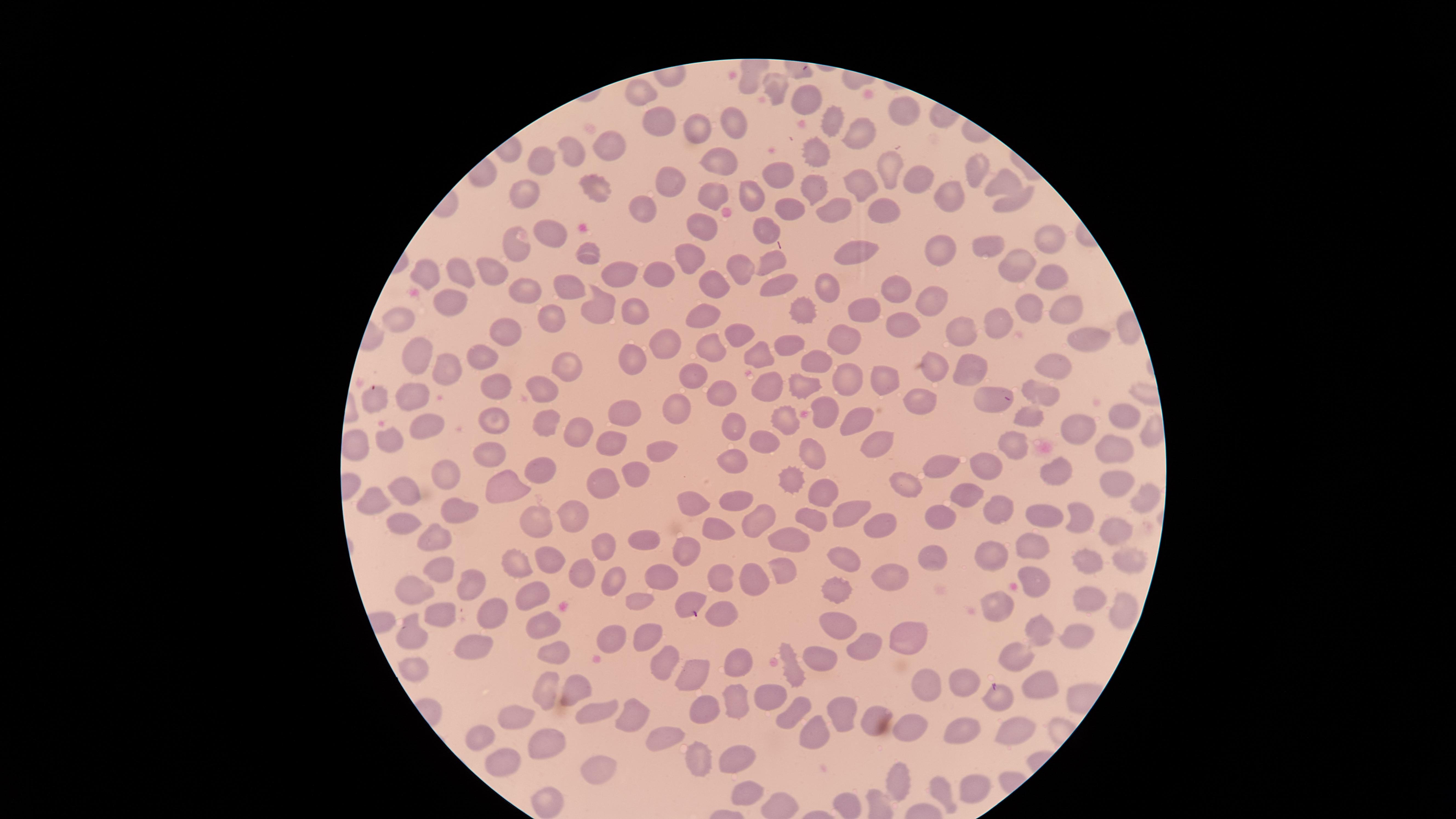

presence: no malaria parasites identified
image_size: 1456×819 pixels
stain: Giemsa
preparation: thin blood smear
visible_region: circular
uninfected_red_blood_cells: 'approximate marker points as {x, y} in pixels: {750, 84}, {776, 87}, {637, 91}, {807, 94}, {905, 111}, {833, 118}, {732, 121}, {661, 123}, {697, 127}, {852, 134}, {569, 148}, {609, 148}, {818, 153}, {542, 158}, {722, 159}, {889, 168}, {777, 169}, {972, 170}, {912, 178}, {667, 182}, {811, 182}, {864, 184}, {1002, 186}, {595, 188}, {748, 192}, {717, 195}, {953, 196}, {525, 199}, {1014, 202}, {830, 204}, {788, 206}, {887, 206}, {648, 208}, {709, 224}, {771, 231}, {548, 236}, {1055, 238}, {520, 243}, {989, 244}, {865, 248}, {590, 253}, {940, 254}, {691, 256}, {775, 257}, {1010, 264}, {491, 267}, {741, 270}, {464, 271}, {427, 272}, {615, 272}, {654, 276}, {717, 282}, {776, 283}, {1053, 283}, {571, 285}, {896, 285}, {526, 286}, {830, 288}, {935, 296}, {595, 304}, {449, 305}, {873, 309}, {638, 310}, {798, 310}, {1064, 312}, {1032, 313}, {706, 315}, {394, 316}, {548, 316}, {894, 321}, {998, 322}, {502, 327}, {738, 332}, {957, 332}, {842, 339}, {1091, 341}, {661, 344}, {716, 344}, {792, 345}, {759, 353}, {484, 358}, {812, 360}, {417, 362}, {560, 362}, {640, 363}, {1047, 363}, {451, 364}, {966, 364}, {936, 370}, {886, 374}, {693, 375}, {545, 380}, {846, 380}, {491, 386}, {804, 386}, {763, 391}, {719, 392}, {1044, 392}, {408, 396}, {989, 396}, {376, 400}, {922, 403}, {623, 411}, {863, 411}, {674, 413}, {827, 416}, {1032, 416}, {492, 417}, {1120, 417}, {779, 419}, {429, 426}, {735, 426}, {575, 428}, {544, 429}, {1081, 433}, {389, 434}, {878, 443}, {1020, 443}, {1113, 445}, {610, 446}, {766, 447}, {812, 448}, {665, 449}, {489, 453}, {730, 461}, {943, 462}, {541, 465}, {984, 465}, {1053, 465}, {639, 474}, {447, 477}, {1115, 478}, {795, 480}, {901, 481}, {608, 485}, {512, 487}, {404, 491}, {822, 494}, {966, 494}, {1147, 496}, {379, 500}, {733, 501}, {691, 502}, {454, 507}, {997, 507}, {852, 509}, {936, 512}, {570, 515}, {1077, 515}, {811, 517}, {404, 518}, {1045, 520}, {534, 522}, {758, 522}, {715, 525}, {880, 530}, {1117, 531}, {434, 536}, {646, 537}, {795, 537}, {597, 544}, {1029, 545}, {686, 551}, {988, 551}, {936, 552}, {1134, 559}, {515, 560}, {550, 560}, {1085, 561}, {847, 562}, {440, 565}, {582, 569}, {780, 570}, {749, 573}, {895, 575}, {665, 576}, {720, 576}, {611, 580}, {1036, 582}, {416, 586}, {471, 587}, {843, 589}, {533, 595}, {631, 598}, {1092, 600}, {688, 601}, {1117, 605}, {996, 607}, {443, 608}, {494, 608}, {722, 608}, {539, 620}, {835, 623}, {1038, 627}, {412, 633}, {913, 636}, {611, 638}, {1080, 639}, {651, 640}, {474, 643}, {860, 645}, {555, 655}, {735, 658}, {1020, 658}, {828, 660}, {663, 662}, {413, 671}, {797, 674}, {697, 676}, {962, 678}, {548, 685}, {1042, 686}, {578, 687}, {924, 688}, {776, 699}, {997, 699}, {734, 701}, {701, 707}, {601, 708}, {632, 710}, {844, 713}, {515, 715}, {874, 717}, {792, 719}, {911, 724}, {1023, 729}, {959, 731}, {662, 735}, {813, 735}, {487, 739}, {544, 743}, {697, 752}, {735, 752}, {507, 757}, {598, 766}, {898, 778}, {940, 788}, {751, 790}, {975, 792}, {548, 799}'
capture: smartphone photograph through the microscope eyepiece
field_of_view: single